Assess this cell for malaria.
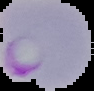
It is parasitized.

From a thin blood film. Segmented cell region on a black background. Image is 94×91 pixels.